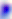

Summary:
  - Identification: Toxoplasma gondii
  - Modality: photomicrograph
  - Magnification: 400x